Classify this cell by malaria status.
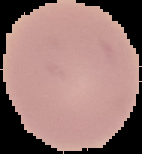
Uninfected.

Summary:
  - Image type: segmented cell region with the area outside set to black
  - Preparation: thin blood film
  - Image size: 142×154 pixels